Give the location of every parasitized RBC.
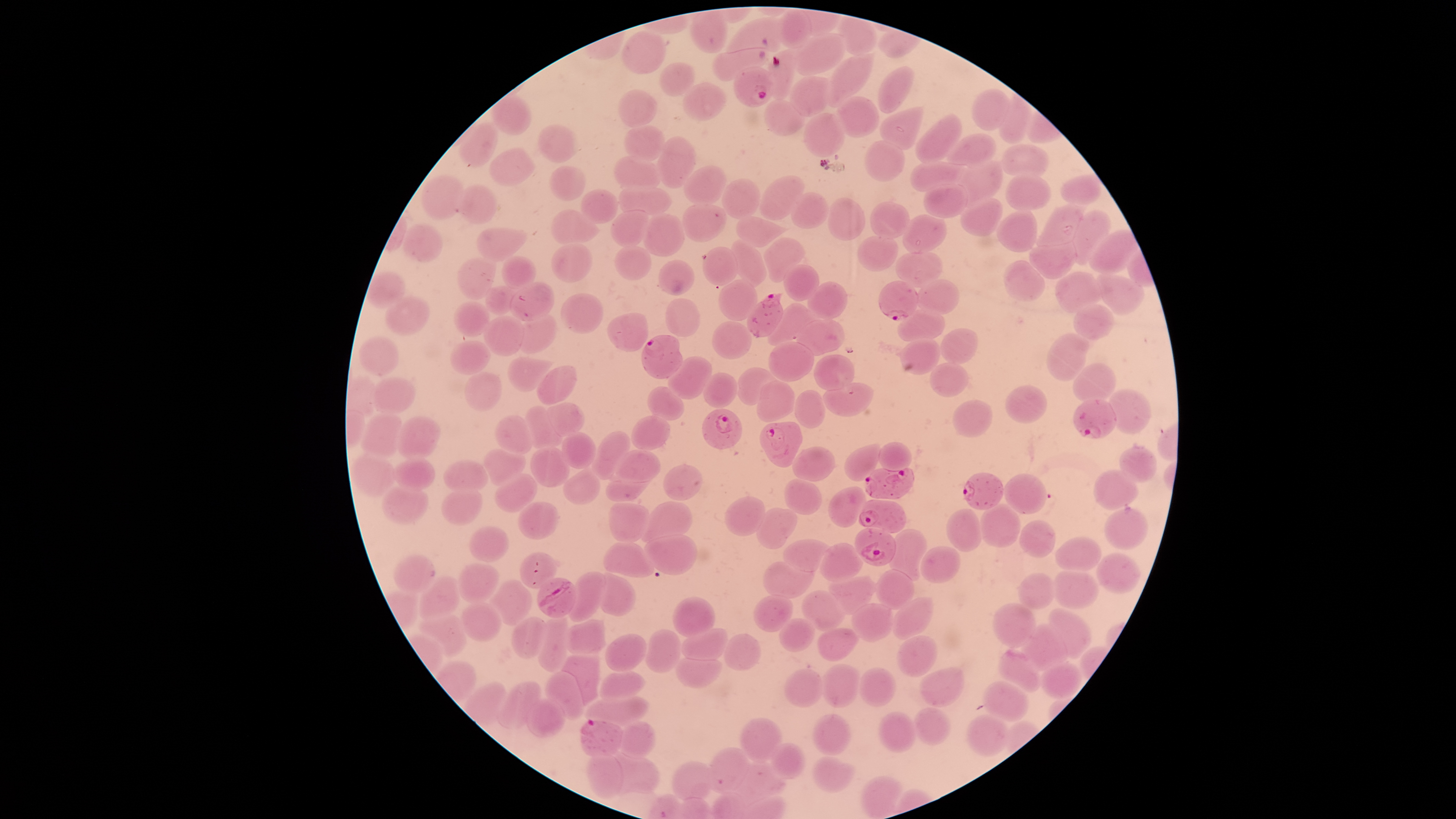

Approximate bounding boxes as [left, top, right, bottom] in pixels.
Parasitized RBCs: [733, 66, 775, 108], [879, 281, 917, 321], [746, 292, 783, 338], [641, 334, 682, 378], [1073, 400, 1117, 438], [702, 408, 743, 450], [759, 422, 802, 468], [864, 468, 916, 499], [964, 472, 1003, 510], [858, 499, 906, 534], [854, 526, 897, 567], [537, 577, 577, 617], [582, 719, 623, 757].

Approximate bounding boxes as [left, top, right, bottom] in pixels. Uninfected RBCs: [777, 9, 810, 48], [690, 11, 727, 53], [726, 17, 781, 53], [623, 31, 666, 73], [793, 34, 847, 76], [712, 48, 768, 80], [763, 49, 796, 100], [827, 53, 875, 106], [660, 62, 696, 95], [878, 66, 913, 113], [788, 75, 831, 117], [682, 82, 726, 122], [973, 89, 1008, 130], [617, 90, 657, 127], [492, 93, 530, 135], [999, 94, 1031, 145], [837, 95, 879, 138], [764, 99, 804, 135], [879, 107, 923, 149], [803, 112, 845, 158], [914, 113, 961, 164], [458, 123, 499, 168], [538, 125, 580, 163], [623, 125, 666, 159], [948, 133, 995, 166], [657, 136, 698, 188], [865, 141, 904, 182], [1001, 145, 1049, 177], [490, 148, 535, 187], [613, 156, 661, 189], [959, 161, 1004, 204], [910, 162, 966, 192], [682, 165, 727, 206], [548, 166, 585, 200], [1061, 174, 1102, 204], [760, 175, 805, 219], [1006, 175, 1052, 211], [421, 176, 464, 221], [721, 178, 760, 219], [922, 182, 967, 218], [458, 184, 497, 223], [617, 187, 672, 216], [581, 189, 618, 225], [791, 192, 829, 229], [828, 198, 866, 240], [960, 198, 1003, 237], [682, 202, 726, 243], [871, 202, 910, 238], [1036, 202, 1084, 247], [550, 209, 598, 246], [995, 209, 1038, 252], [611, 210, 649, 246], [1070, 210, 1112, 264], [642, 214, 685, 258], [903, 214, 948, 254], [736, 216, 790, 248], [402, 225, 443, 261], [477, 228, 528, 258], [1090, 229, 1139, 274], [857, 236, 899, 272], [763, 237, 805, 283], [731, 239, 766, 287], [1028, 241, 1075, 278], [551, 243, 592, 283], [615, 246, 651, 281], [703, 247, 737, 285], [896, 251, 943, 288], [501, 256, 537, 289], [458, 258, 496, 300], [658, 260, 694, 296], [1003, 260, 1045, 302], [784, 264, 819, 301], [366, 271, 404, 308], [1054, 272, 1101, 315], [1096, 275, 1145, 315], [718, 279, 757, 321], [917, 279, 960, 315], [809, 281, 847, 319], [508, 282, 555, 322], [484, 285, 520, 315], [560, 293, 604, 335], [385, 297, 429, 336], [665, 298, 700, 338], [453, 302, 490, 336], [1072, 303, 1114, 340], [767, 304, 810, 346], [897, 309, 944, 341], [515, 313, 557, 355], [607, 313, 648, 351], [482, 316, 525, 357], [797, 319, 845, 355], [712, 321, 752, 359], [940, 328, 977, 364], [1046, 334, 1089, 382], [359, 337, 397, 375], [899, 338, 940, 375], [450, 341, 490, 375], [768, 342, 814, 381], [814, 354, 854, 390], [667, 356, 711, 401], [508, 358, 555, 393], [930, 363, 969, 398], [1072, 363, 1118, 403], [536, 366, 577, 406], [737, 367, 778, 406], [463, 372, 502, 411], [704, 373, 737, 408], [371, 377, 417, 415], [756, 381, 795, 422], [822, 382, 873, 417], [1006, 385, 1048, 424], [647, 386, 685, 421], [1109, 389, 1151, 434], [794, 390, 825, 429], [954, 400, 992, 436], [549, 402, 586, 437], [525, 405, 562, 449], [360, 415, 402, 457], [398, 415, 439, 460], [494, 415, 533, 454], [631, 415, 671, 450], [592, 431, 631, 481], [562, 432, 596, 469], [878, 442, 912, 472], [845, 443, 880, 482], [791, 446, 834, 483], [1119, 446, 1156, 483], [482, 447, 525, 485], [529, 447, 569, 488], [609, 449, 660, 483], [351, 453, 396, 496], [393, 457, 434, 491], [440, 460, 488, 492], [662, 465, 704, 500], [563, 468, 600, 506], [1095, 469, 1137, 511], [493, 473, 538, 513], [1003, 475, 1047, 513], [604, 478, 654, 501], [784, 480, 822, 514], [381, 485, 428, 526], [439, 487, 482, 526], [830, 487, 866, 526], [724, 497, 765, 535], [641, 501, 693, 542], [517, 503, 559, 539], [608, 503, 650, 544], [979, 504, 1020, 547], [1104, 506, 1148, 550], [756, 508, 797, 549], [947, 509, 982, 550], [1019, 521, 1055, 558], [468, 526, 508, 563], [889, 529, 926, 580], [646, 534, 697, 575], [1056, 537, 1101, 572], [783, 539, 833, 571], [603, 542, 654, 577], [819, 544, 863, 582], [918, 547, 959, 583], [520, 553, 557, 589], [1096, 553, 1139, 593], [394, 555, 435, 593], [762, 562, 816, 596], [456, 564, 498, 604], [1053, 569, 1099, 609], [875, 570, 914, 609], [568, 572, 605, 622], [601, 572, 634, 616], [1018, 572, 1054, 610], [420, 574, 460, 620], [830, 575, 876, 615], [491, 580, 531, 626], [802, 590, 849, 632], [754, 594, 793, 632], [672, 596, 716, 637], [891, 598, 933, 640], [460, 602, 500, 643], [851, 603, 892, 642], [991, 604, 1036, 649], [1049, 608, 1091, 660], [418, 612, 466, 658], [537, 616, 569, 672], [511, 617, 545, 658], [778, 619, 815, 652], [564, 620, 605, 656], [1022, 624, 1066, 670], [681, 628, 729, 660], [816, 629, 858, 662], [645, 630, 681, 674], [723, 633, 761, 670], [606, 634, 646, 672], [897, 635, 937, 677], [999, 650, 1041, 691], [559, 654, 599, 707], [674, 657, 723, 689], [1042, 662, 1080, 699], [823, 664, 861, 706], [859, 667, 896, 706], [920, 667, 964, 705], [787, 669, 822, 707], [545, 671, 586, 719], [599, 671, 645, 701], [496, 681, 540, 728], [983, 681, 1029, 723], [582, 696, 649, 729], [526, 699, 565, 738], [913, 707, 952, 746], [878, 711, 917, 753], [967, 714, 1010, 757], [812, 715, 850, 756], [739, 718, 782, 762], [619, 721, 656, 756], [765, 743, 805, 779], [707, 748, 750, 792], [611, 752, 658, 795], [585, 754, 623, 797], [812, 756, 855, 792], [672, 761, 712, 800], [729, 761, 785, 803], [860, 775, 902, 819]. Thin blood smear. Image is 1456×819 pixels. One field of view of the specimen. Species: Plasmodium falciparum. Giemsa stain. Smartphone photograph through the microscope eyepiece. Circular visible region.